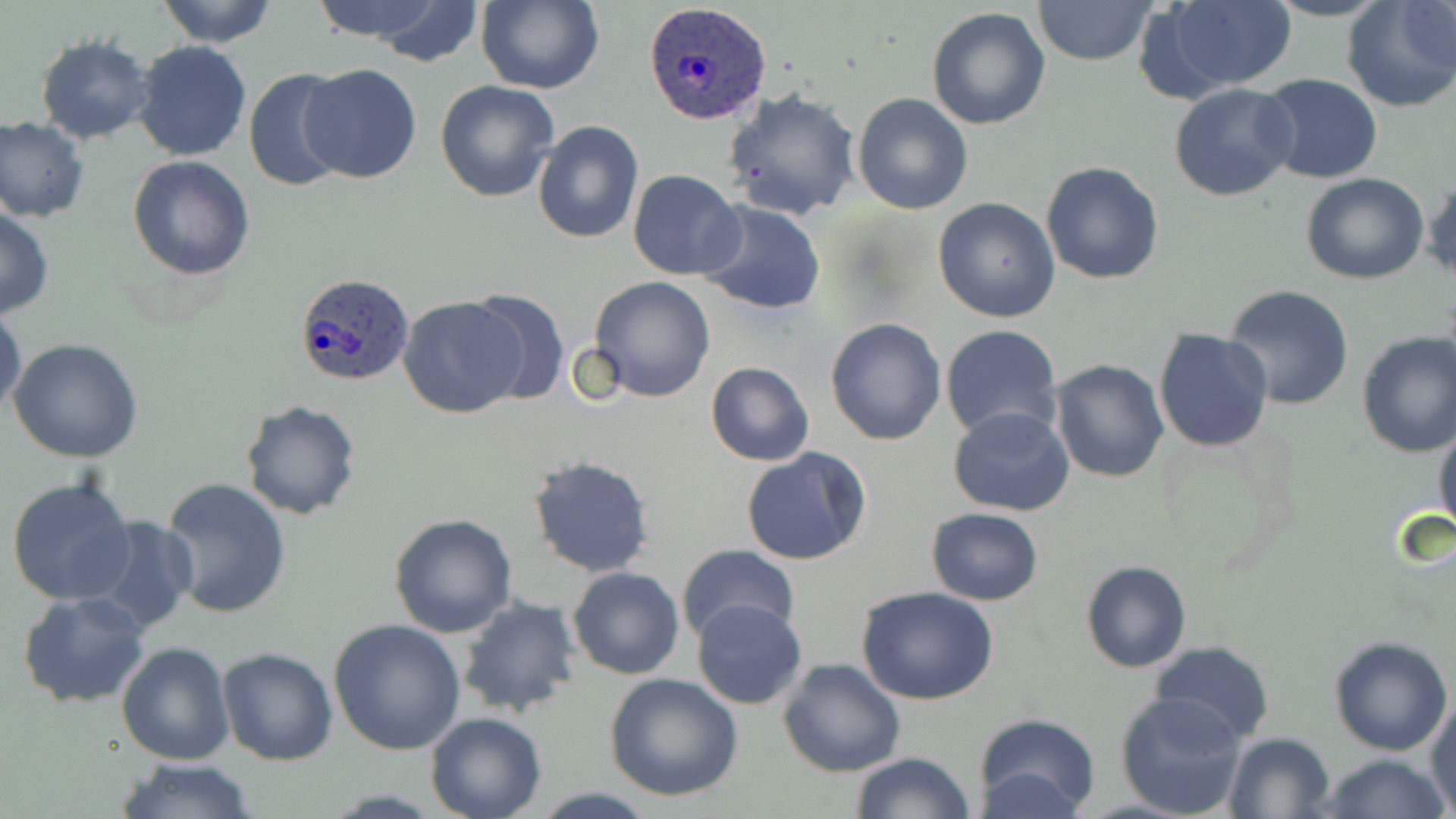
{
  "slide_level_diagnosis": "Plasmodium ovale",
  "magnification": "1000x",
  "modality": "optical microscopy",
  "plasmodium_ovale_infected_red_blood_cell_locations": "approximate bounding boxes as [x1, y1, x2, y2] in pixels: [644, 2, 773, 123], [294, 271, 415, 385]",
  "uninfected_red_blood_cell_locations": "approximate bounding boxes as [x1, y1, x2, y2] in pixels: [155, 0, 279, 47], [318, 0, 486, 66], [475, 0, 604, 94], [1031, 0, 1159, 66], [1145, 0, 1297, 97], [1262, 0, 1394, 21], [1342, 1, 1456, 114], [926, 8, 1051, 130], [35, 34, 156, 144], [132, 41, 253, 163], [296, 64, 423, 183], [243, 65, 357, 193], [1257, 72, 1383, 183], [435, 81, 561, 202], [1168, 82, 1299, 202], [722, 89, 862, 222], [852, 91, 973, 215], [0, 116, 89, 222], [532, 120, 644, 244], [127, 156, 255, 279], [1041, 161, 1164, 284], [627, 169, 745, 280], [1300, 172, 1430, 284], [1424, 177, 1456, 287], [932, 197, 1060, 322], [694, 200, 827, 316], [0, 205, 53, 319], [588, 276, 715, 403], [1222, 283, 1354, 410], [461, 286, 572, 405], [398, 296, 528, 418], [0, 302, 26, 420], [825, 317, 946, 446], [940, 325, 1064, 444], [1153, 327, 1274, 450], [1355, 331, 1456, 458], [8, 339, 145, 463], [1049, 359, 1170, 483], [705, 361, 815, 467], [240, 400, 362, 519], [948, 407, 1076, 515], [1433, 422, 1456, 542], [741, 448, 871, 566], [527, 454, 656, 577], [7, 474, 139, 607], [160, 476, 292, 620], [927, 507, 1043, 605], [389, 512, 518, 638], [85, 515, 201, 634], [676, 543, 798, 646], [1082, 560, 1191, 673], [566, 565, 685, 680], [857, 585, 999, 705], [18, 591, 152, 710], [458, 596, 581, 718], [692, 598, 807, 710], [329, 620, 465, 756], [1329, 635, 1453, 756], [1149, 641, 1274, 744], [116, 642, 235, 766], [216, 647, 340, 765], [778, 658, 905, 775], [603, 672, 743, 801], [1115, 693, 1249, 819], [1427, 695, 1456, 814], [426, 710, 546, 819], [973, 713, 1098, 817], [1223, 732, 1336, 818], [850, 752, 974, 819], [1318, 753, 1449, 819], [112, 759, 258, 818]",
  "stain": "May-Grünwald-Giemsa",
  "field_of_view": "single",
  "preparation": "thin blood smear",
  "image_size": "1456×819 pixels"
}